Assess the morphology of the red blood cells.
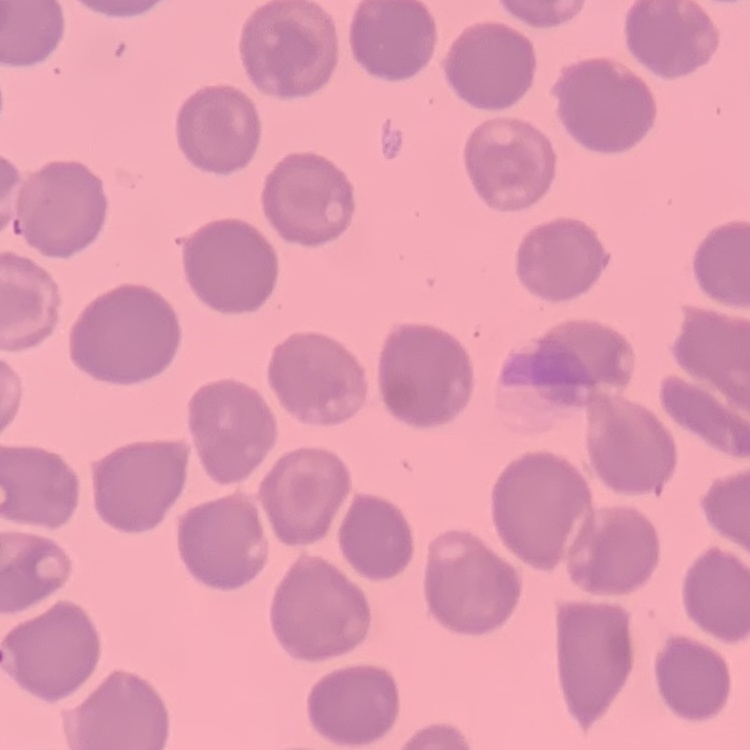
No rouleaux formation.

One tile cut from a larger photomicrograph. Thin peripheral smear. Stained with either Field's or Giemsa.